Point out each Plasmodium parasite.
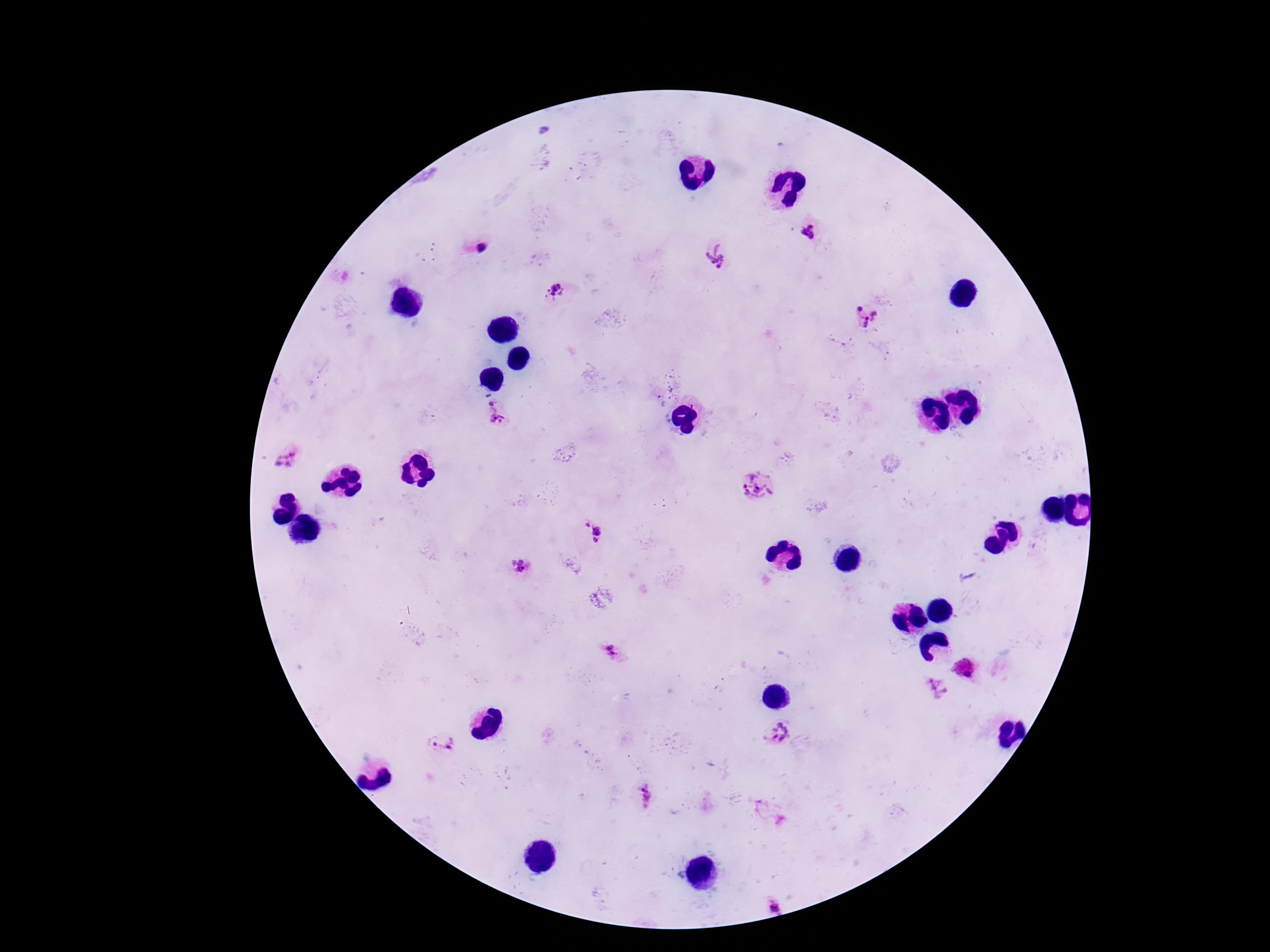

Approximate centers as {x, y} in pixels.
Plasmodium parasites: {809, 232}, {480, 249}, {715, 255}, {557, 292}, {864, 316}, {492, 403}, {497, 419}, {289, 458}, {757, 485}, {592, 531}, {521, 567}, {610, 650}, {937, 687}, {779, 734}, {442, 743}, {646, 796}, {774, 902}.

stain = Giemsa
preparation = thick peripheral-blood smear
patient malaria status = positive
field of view = single
capture = smartphone camera through the microscope eyepiece
magnification = 100x
image size = 1270×952 pixels